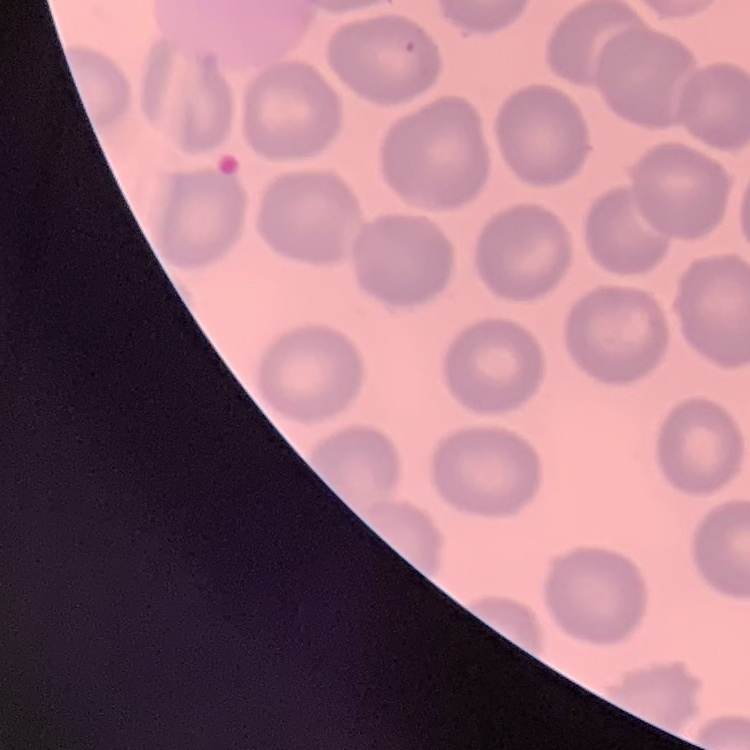 The erythrocytes show no rouleaux formation. Field's or Giemsa stain. Thin blood smear. Square crop of a larger photomicrograph.